Classify this cell by malaria status.
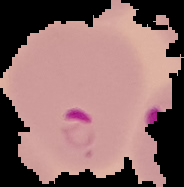
Parasitized.

From a thin blood film. Cell region segmented out of the field of view; the surrounding area is masked to black. Image is 184×187 pixels.